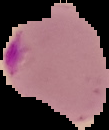

Result: Plasmodium parasites detected. From a thin blood smear. Cell region segmented out of the field of view; the surrounding area is masked to black. Image is 109×130 pixels.